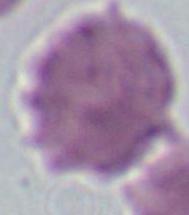 Micrograph. A red blood cell is seen. Captured at 1000x magnification.